Name the blood parasite species.
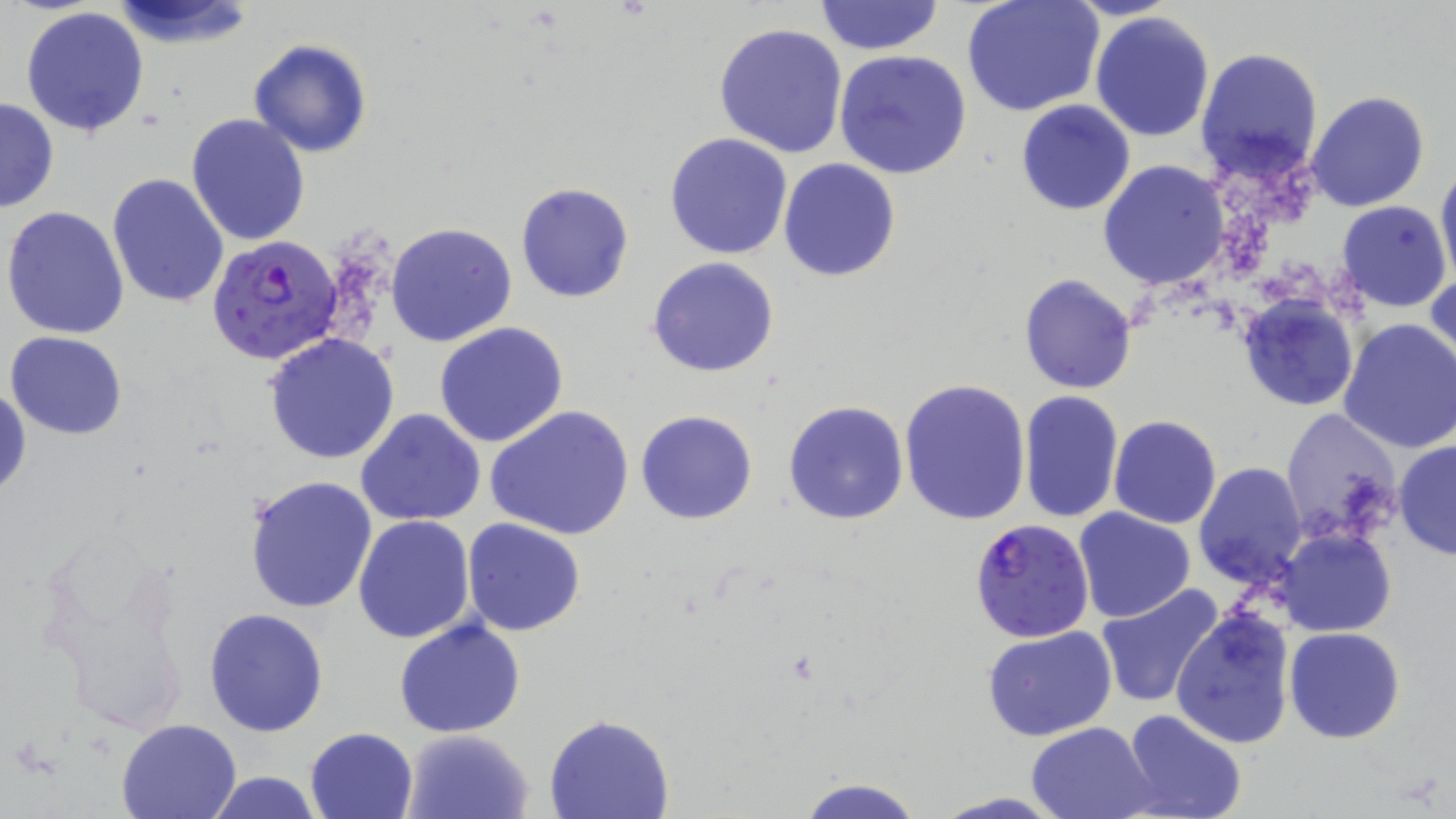
Plasmodium falciparum.

Approximate bounding boxes as (x1,y1)-(x2,y2) corner pairs in pixels. Plasmodium falciparum-infected red blood cell locations: (207,235)-(344,364), (970,522)-(1096,645). Uninfected red blood cell locations: (108,0)-(259,48), (815,0)-(944,56), (961,0)-(1105,118), (21,6)-(150,138), (1090,12)-(1216,142), (714,21)-(848,158), (248,37)-(373,158), (833,48)-(972,179), (1195,48)-(1324,183), (1306,90)-(1430,212), (0,95)-(59,214), (1016,99)-(1136,214), (185,113)-(311,247), (664,132)-(794,260), (778,157)-(902,282), (1099,160)-(1229,291), (1435,161)-(1456,288), (107,173)-(231,308), (516,181)-(634,302), (1337,200)-(1452,312), (2,205)-(131,340), (386,222)-(517,347), (648,257)-(779,378), (1426,271)-(1456,382), (1018,274)-(1137,394), (1238,296)-(1358,413), (1236,305)-(1456,430), (1337,318)-(1456,454), (434,322)-(568,448), (5,330)-(128,439), (265,333)-(400,464), (899,378)-(1032,526), (1,381)-(29,501), (1019,390)-(1123,524), (783,400)-(909,524), (488,405)-(634,542), (1281,408)-(1404,547), (356,409)-(486,527), (636,410)-(758,525), (1109,416)-(1221,529), (1393,440)-(1456,561), (1193,461)-(1307,589), (246,474)-(379,614), (1075,509)-(1197,623), (353,515)-(475,643), (462,518)-(588,637), (1277,528)-(1394,636), (1095,584)-(1224,707), (204,607)-(329,737), (1171,607)-(1295,749), (393,618)-(526,739), (981,627)-(1118,743), (1285,627)-(1404,744), (1123,710)-(1248,819), (544,714)-(674,819), (114,717)-(241,819), (1027,720)-(1159,819), (304,726)-(418,818), (402,729)-(535,819), (203,771)-(327,819), (796,777)-(925,819), (931,792)-(1069,819). May-Grünwald-Giemsa-stained preparation. Single field of view. Thin blood smear. Captured at 1000x magnification. Optical microscopy. Image is 1456×819 pixels.